Name the parasite shown.
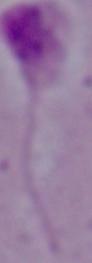
This is Leishmania.

Summary:
  - Modality: micrograph
  - Magnification: 1000x